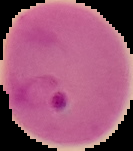
malaria status = parasitized
image size = 133×151 pixels
image type = cell region segmented out of the field of view; surrounding area masked to black
preparation = thin blood smear